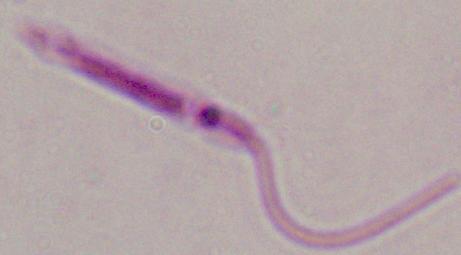

identification: Leishmania
magnification: 1000x
modality: micrograph